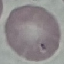

Malaria status: uninfected. Thin blood smear. Photographed with a smartphone camera at the microscope eyepiece. Automatically extracted cell patch, resized to 64 × 64 pixels. Giemsa-stained preparation.